Report the malaria status of this cell.
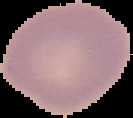

It is uninfected.

Summary:
  - Image type: cell region segmented out of the field of view; surrounding area masked to black
  - Image size: 133×118 pixels
  - Preparation: thin blood smear